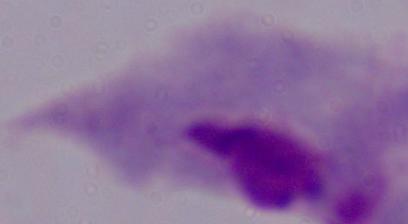

A trichomonad is shown. Micrograph. Captured at 1000x magnification.